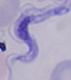
Summary:
  - Identification: trypanosome
  - Modality: photomicrograph
  - Magnification: 1000x